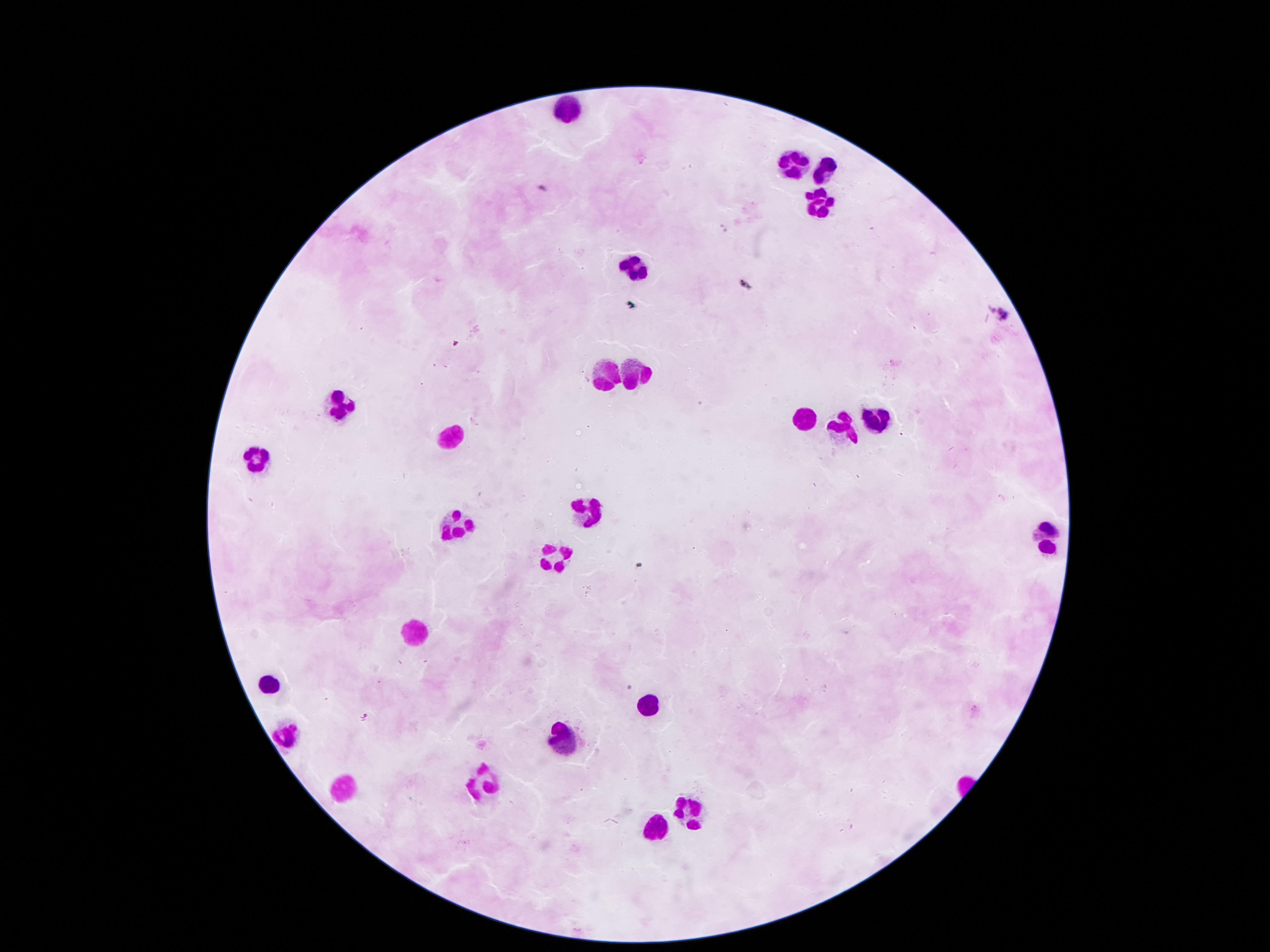

Approximate centers as {x, y} in pixels.
Summary:
  - Leukocyte locations: {569, 108}, {794, 165}, {825, 173}, {816, 198}, {631, 265}, {608, 371}, {635, 373}, {338, 408}, {877, 418}, {805, 420}, {841, 428}, {444, 435}, {250, 457}, {590, 507}, {454, 525}, {1047, 538}, {553, 557}, {417, 629}, {270, 687}, {652, 708}, {285, 737}, {560, 737}, {481, 783}, {342, 787}, {686, 806}, {657, 830}
  - Preparation: thick peripheral-blood smear
  - Capture: smartphone camera through the microscope eyepiece
  - Magnification: 100x
  - Field of view: one from this slide
  - Patient malaria status: uninfected
  - Stain: Giemsa
  - Image size: 1270×952 pixels